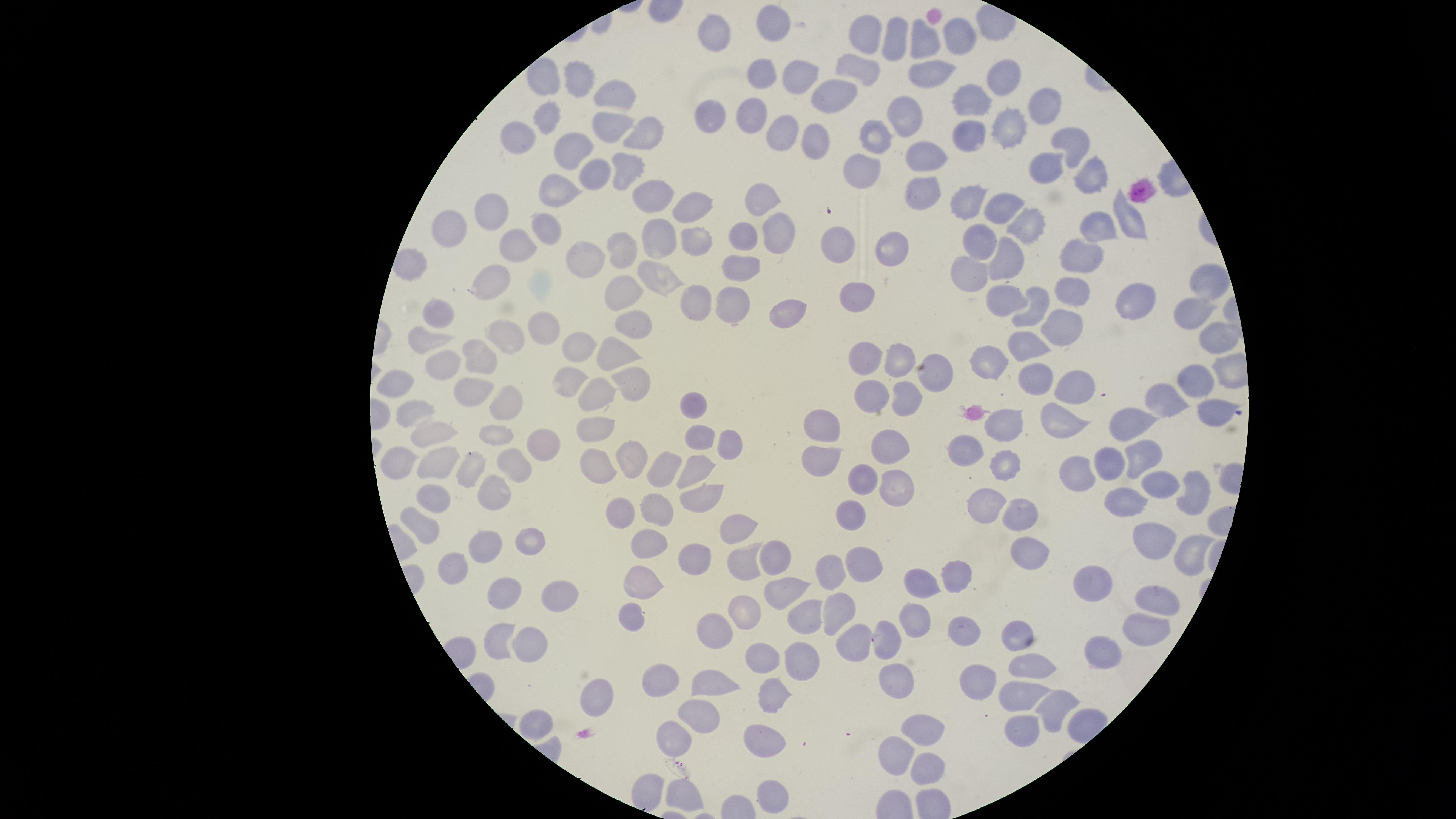
Approximate marker points as [x, y] in pixels. Uninfected red blood cells: [769, 25], [714, 32], [867, 32], [894, 38], [959, 39], [926, 42], [867, 64], [928, 71], [761, 73], [798, 74], [543, 77], [1002, 77], [577, 78], [838, 92], [619, 93], [973, 96], [1043, 107], [754, 112], [710, 113], [901, 114], [548, 118], [1009, 125], [611, 128], [776, 129], [636, 133], [877, 134], [966, 135], [522, 136], [820, 137], [1073, 140], [577, 150], [925, 150], [631, 165], [1043, 165], [866, 166], [592, 174], [1087, 174], [926, 187], [560, 194], [656, 194], [759, 197], [967, 200], [994, 205], [692, 208], [489, 209], [1132, 217], [449, 221], [1025, 222], [1098, 223], [543, 228], [775, 233], [659, 234], [698, 238], [744, 239], [833, 243], [983, 243], [517, 245], [616, 248], [888, 248], [1007, 257], [1083, 257], [582, 260], [743, 264], [968, 273], [660, 277], [489, 278], [1206, 280], [628, 285], [1073, 286], [857, 294], [725, 299], [1127, 299], [695, 301], [1010, 302], [1036, 310], [773, 312], [1191, 312], [435, 321], [1059, 324], [638, 326], [539, 330], [1216, 336], [428, 341], [507, 341], [1025, 344], [577, 347], [609, 351], [480, 353], [900, 360], [868, 361], [989, 363], [442, 365], [1200, 376], [636, 378], [937, 380], [1036, 380], [568, 386], [396, 387], [1078, 388], [872, 394], [471, 395], [598, 397], [1166, 400], [904, 401], [693, 402], [513, 407], [1209, 407], [412, 413], [1062, 417], [1009, 420], [1135, 421], [592, 425], [827, 427], [435, 431], [498, 431], [698, 436], [539, 444], [727, 445], [888, 445], [968, 450], [627, 454], [1145, 455], [820, 457], [400, 458], [1113, 460], [696, 462], [1004, 462], [436, 464], [475, 464], [662, 464], [596, 465], [513, 466], [1078, 472], [862, 477], [898, 484], [1155, 486], [1195, 487], [495, 494], [698, 494], [434, 498], [1126, 506], [983, 508], [653, 510], [848, 510], [1020, 510], [619, 511], [738, 525], [420, 526], [533, 538], [647, 538], [489, 539], [1144, 541], [1026, 546], [1189, 556], [778, 557], [741, 558], [692, 560], [862, 562], [834, 563], [455, 567], [962, 573], [644, 577], [921, 580], [1095, 580], [788, 585], [502, 589], [551, 595], [1152, 597], [838, 607], [809, 610], [745, 613], [912, 615], [631, 616], [716, 625], [1146, 627], [1023, 629], [960, 632], [526, 635], [500, 637], [852, 641], [889, 641], [1101, 651], [763, 654], [800, 654], [1034, 661], [714, 680], [980, 680], [654, 682], [897, 682], [602, 694], [771, 695], [1019, 695], [1054, 703], [697, 715], [538, 721], [1022, 729], [922, 731], [676, 738], [760, 739], [897, 754], [925, 767], [645, 787], [769, 795], [682, 796]. Giemsa stain. Circular visible region. Image is 1456×819 pixels. Single field of view. Thin blood film. Presence: no malaria parasites detected. Photographed with a smartphone camera through the microscope eyepiece.